Name the cell type shown.
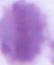
This is an erythrocyte.

{
  "modality": "micrograph",
  "magnification": "1000x"
}